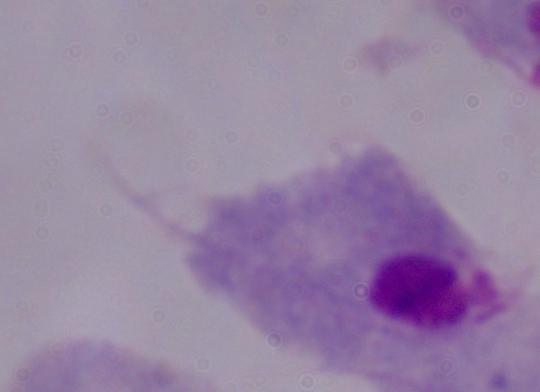

Summary:
  - Magnification: 1000x
  - Modality: micrograph
  - Identification: trichomonad